Give the position of every malaria parasite.
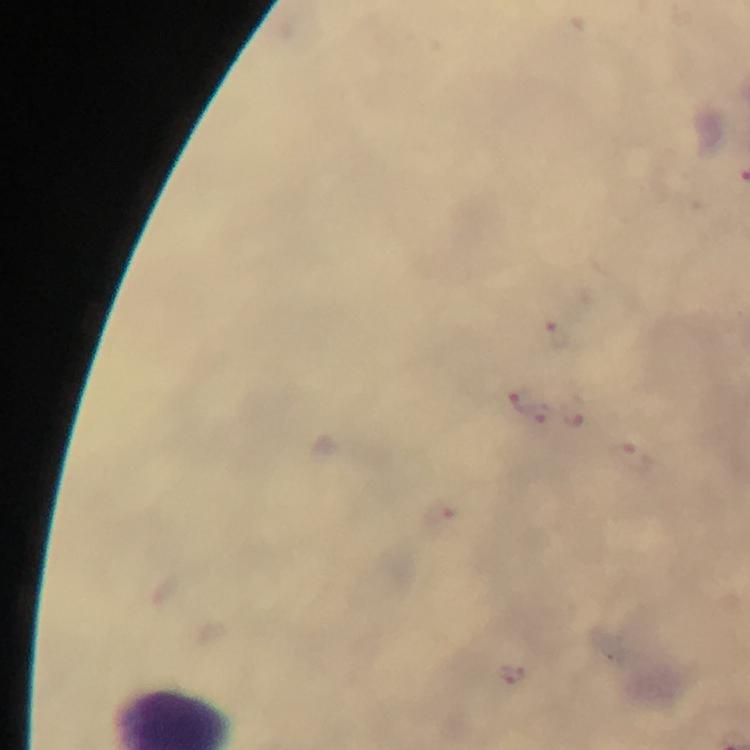
Approximate centers as [x, y] in pixels.
Malaria parasites: [558, 333], [523, 401], [637, 458], [441, 517], [512, 674].

Immersion oil was used. Giemsa-stained preparation. A crop from one field of view. At 100x magnification. Smartphone photograph taken through a microscope. Thick blood film. Image is 750×750 pixels. From a malaria diagnostic workup.